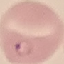
Malaria status: parasitized. Photographed with a smartphone camera at the microscope eyepiece. Giemsa-stained preparation. Automatically extracted cell patch, resized to 64 × 64 pixels. Thin smear of blood.